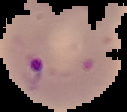

Summary:
  - Preparation: thin blood film
  - Image size: 127×112 pixels
  - Malaria status: parasitized
  - Image type: segmented cell region with the area outside set to black